Describe the morphology of the erythrocytes.
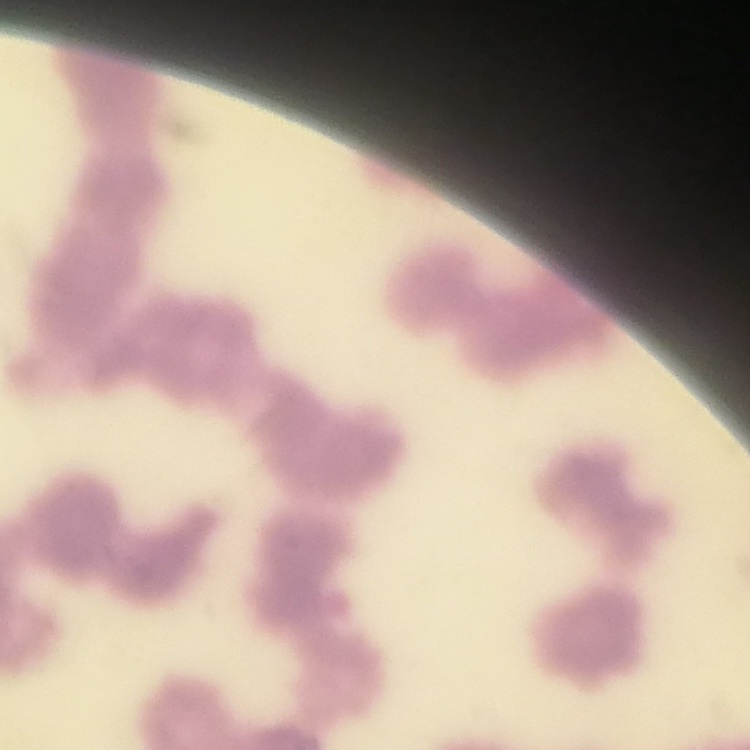

Rouleaux formation.

Summary:
  - Image type: square crop of a larger photomicrograph
  - Stain: Field's or Giemsa
  - Preparation: thin blood film